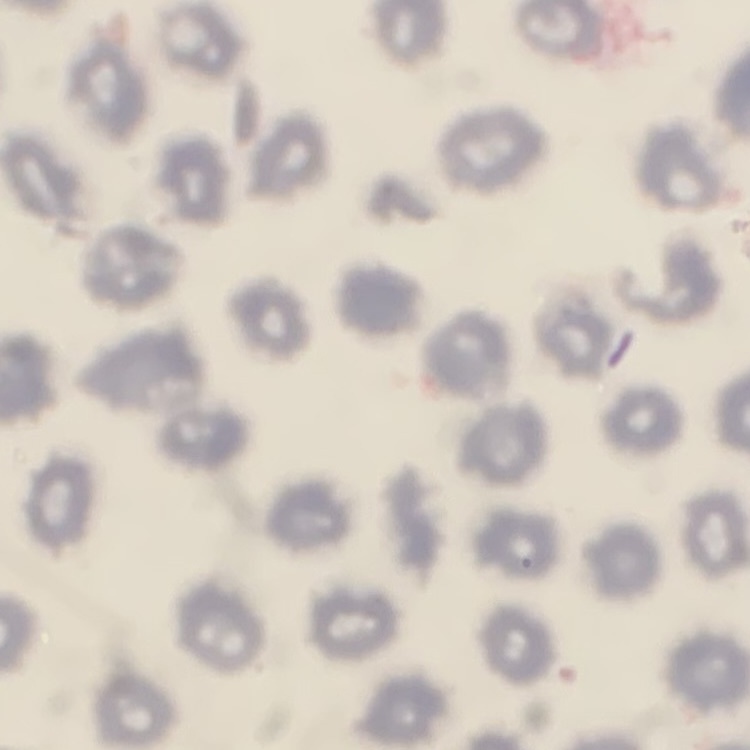

The red blood cells exhibit no rouleaux formation. Thin blood film. One tile cut from a larger photomicrograph. Stained with either Field's or Giemsa.